State which parasite is depicted.
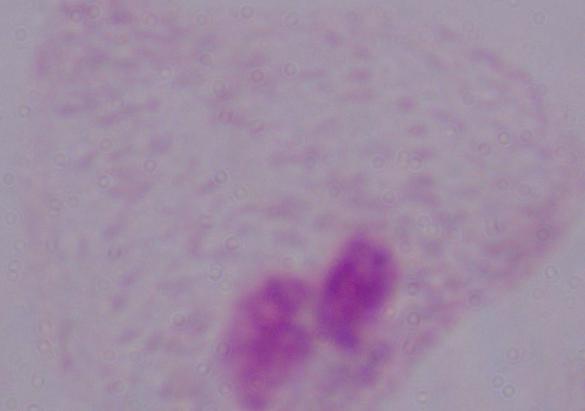
This is a trichomonad.

Micrograph. 1000x magnification.